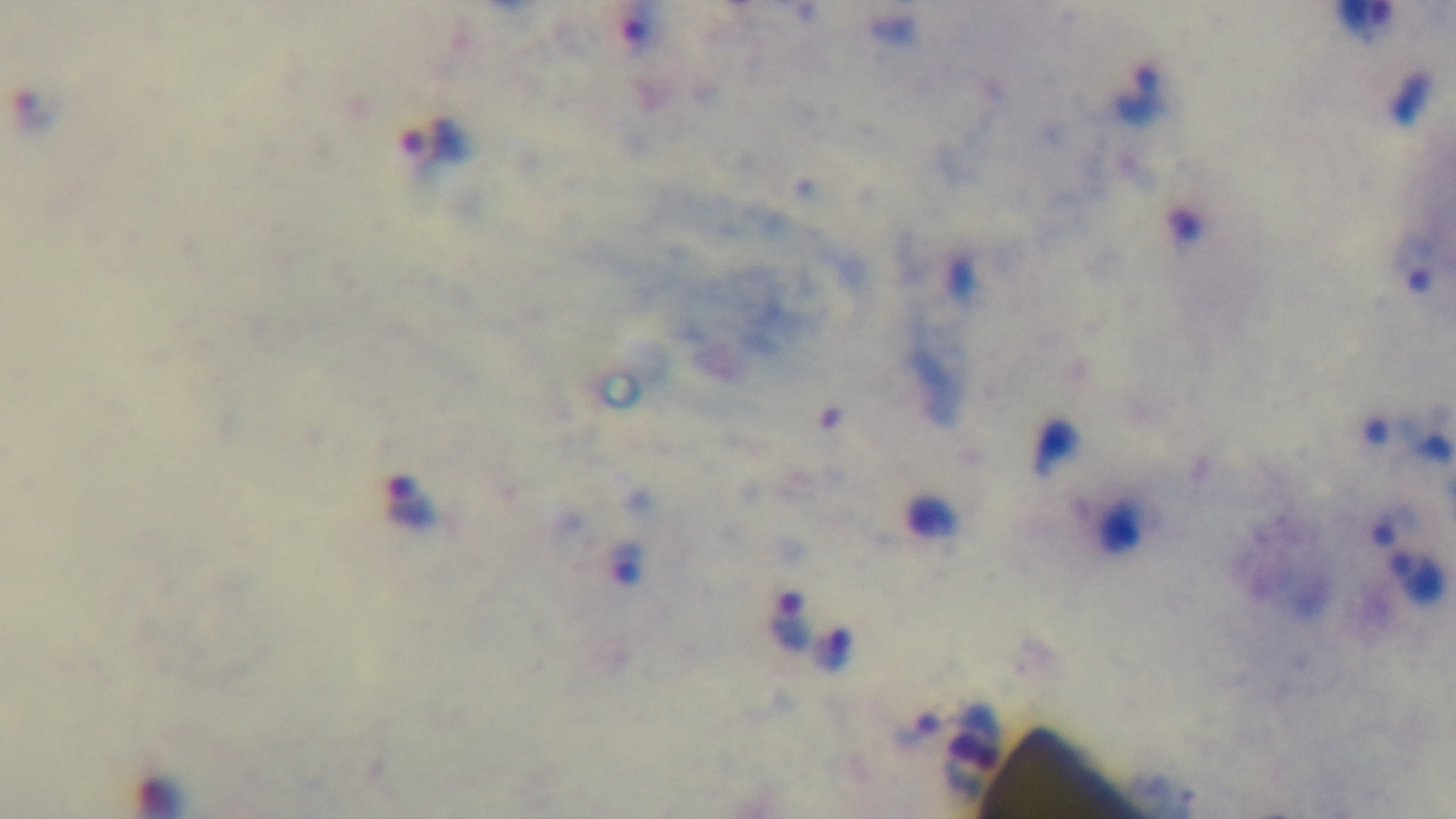
Summary:
  - Capture: mounted 4K digital camera
  - Objective: 100x oil immersion
  - Stain: Giemsa
  - Modality: light microscopy
  - Malaria status: infected
  - Field of view: one from the slide
  - Preparation: thick